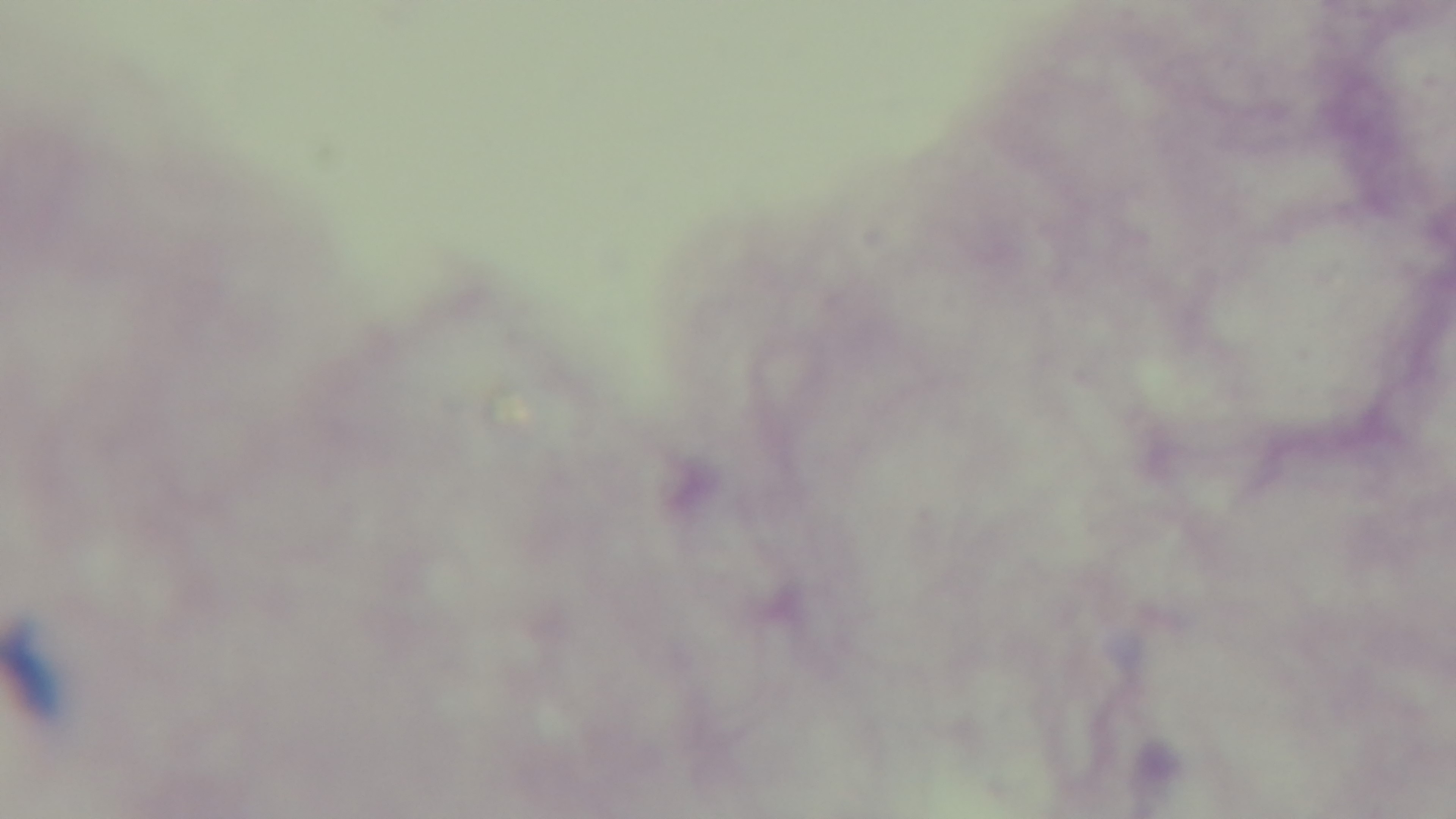

Summary:
  - Objective: 100x oil immersion
  - Preparation: thick
  - Modality: light microscopy
  - Field of view: one from the slide
  - Malaria status: uninfected
  - Capture: mounted 4K digital camera
  - Stain: Giemsa